Classify this cell by malaria status.
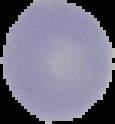
It is uninfected.

preparation: thin blood film
image_size: 115×124 pixels
image_type: segmented cell region on a black background